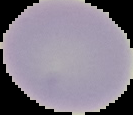

Image is 133×115 pixels. From a thin blood smear. Result: negative for Plasmodium parasites. Cell region segmented out of the field of view; the surrounding area is masked to black.